Locate every malaria parasite.
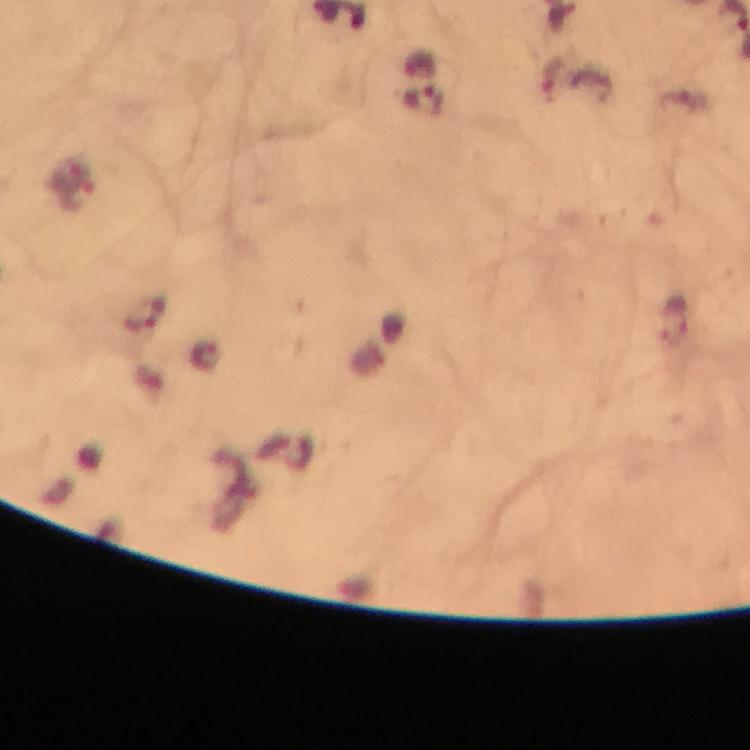
Approximate object centers, in pixels from the top-left corner.
Malaria parasites: (x=550, y=79), (x=424, y=102), (x=71, y=172), (x=79, y=197), (x=147, y=317), (x=676, y=317).

immersion oil = used
cropped from = a single field of view
context = from a malaria diagnostic workup
magnification = 100x
capture = smartphone camera through the microscope
stain = Giemsa
image size = 750×750 pixels
preparation = thick smear